Outline each blood parasite and name the species.
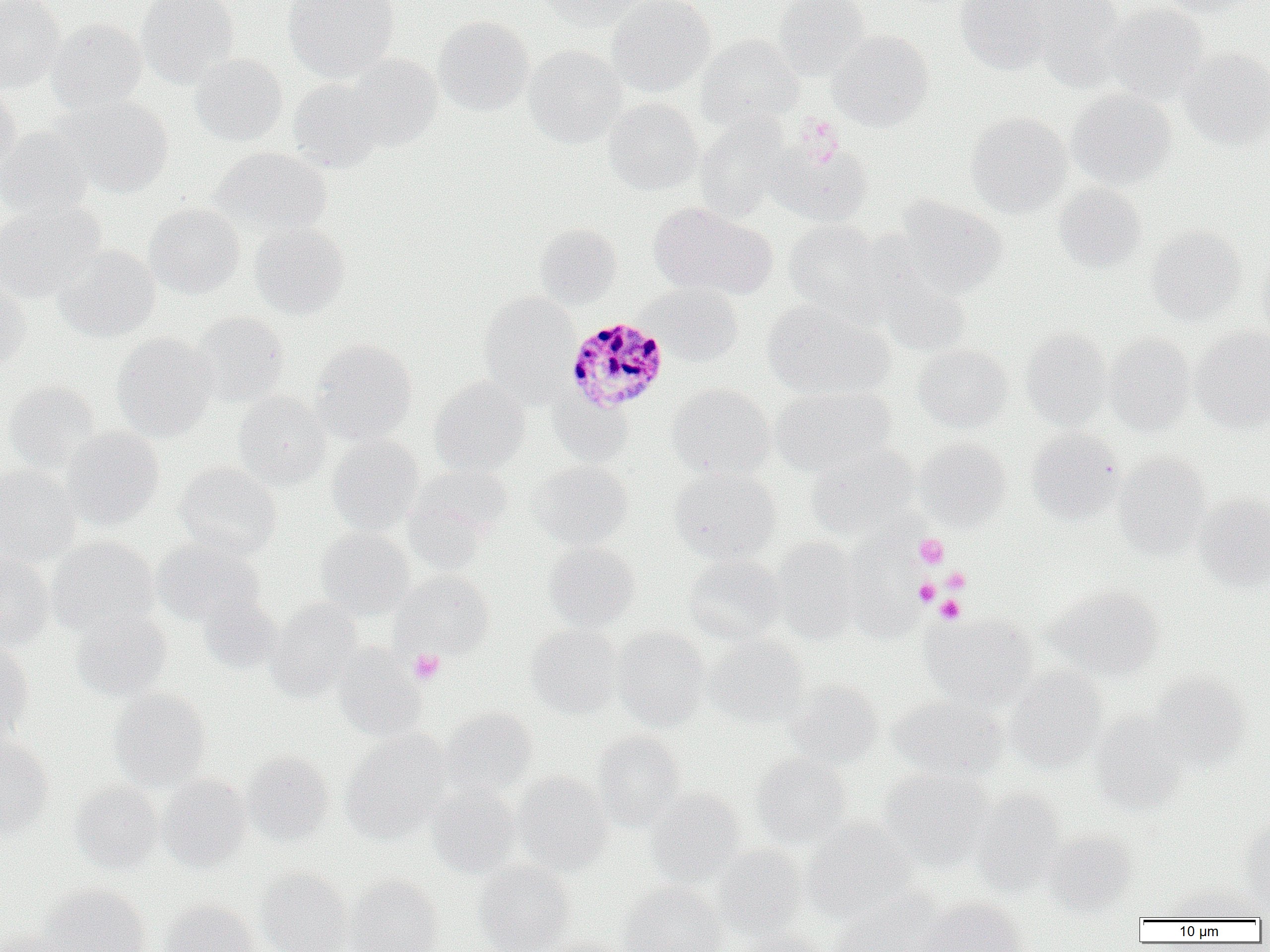

Approximate bounding boxes as [x1, y1, x2, y2] in pixels.
Plasmodium malariae-infected red blood cells: [565, 316, 669, 414].
No Plasmodium falciparum, Plasmodium ovale, Plasmodium vivax, Babesia divergens, or Trypanosoma brucei observed.

Platelet locations: [795, 116, 845, 166], [914, 533, 949, 569], [941, 568, 970, 593], [914, 578, 939, 606], [935, 596, 964, 623], [409, 648, 445, 684]. Uninfected red blood cell locations: [0, 0, 64, 94], [135, 0, 240, 88], [282, 0, 400, 82], [536, 0, 651, 29], [606, 0, 716, 97], [773, 0, 870, 81], [956, 0, 1053, 74], [1029, 0, 1126, 88], [1159, 0, 1263, 17], [1102, 3, 1209, 105], [433, 17, 534, 116], [48, 19, 147, 113], [828, 30, 933, 130], [696, 34, 803, 130], [524, 45, 628, 148], [1179, 48, 1270, 150], [189, 54, 287, 146], [344, 55, 443, 152], [287, 78, 384, 172], [0, 84, 21, 176], [1067, 89, 1176, 190], [53, 96, 173, 197], [603, 98, 703, 195], [966, 111, 1071, 217], [696, 115, 792, 221], [0, 127, 95, 220], [770, 140, 873, 226], [210, 146, 331, 237], [1054, 183, 1147, 272], [894, 197, 1008, 297], [0, 200, 105, 303], [649, 201, 775, 300], [145, 203, 245, 298], [783, 219, 888, 318], [249, 222, 349, 319], [534, 223, 621, 309], [1147, 226, 1247, 325], [53, 245, 159, 342], [1256, 249, 1270, 341], [0, 276, 31, 368], [876, 276, 973, 357], [641, 282, 744, 366], [478, 292, 579, 400], [763, 300, 894, 400], [191, 312, 289, 407], [1191, 326, 1270, 430], [1021, 329, 1112, 430], [112, 332, 218, 441], [1104, 333, 1196, 435], [311, 339, 417, 444], [913, 343, 1013, 431], [430, 376, 530, 476], [3, 380, 100, 474], [666, 383, 775, 480], [771, 386, 896, 476], [233, 390, 331, 490], [551, 393, 633, 466], [60, 427, 164, 529], [1027, 429, 1123, 524], [326, 435, 424, 536], [914, 438, 1011, 530], [807, 444, 919, 540], [1112, 454, 1212, 556], [531, 460, 633, 550], [175, 462, 281, 558], [0, 465, 81, 566], [410, 465, 514, 545], [669, 467, 781, 565], [402, 491, 493, 571], [1195, 494, 1270, 590], [316, 528, 413, 619], [47, 535, 160, 636], [153, 537, 265, 626], [771, 537, 862, 645], [840, 539, 925, 642], [544, 542, 640, 630], [0, 552, 54, 652], [683, 555, 786, 645], [392, 570, 494, 658], [1046, 585, 1164, 681], [198, 595, 282, 674], [266, 598, 363, 701], [70, 609, 172, 701], [924, 613, 1037, 709], [526, 624, 623, 717], [613, 627, 710, 731], [705, 635, 809, 728], [0, 640, 34, 741], [332, 646, 426, 741], [1005, 666, 1107, 770], [1149, 673, 1251, 771], [785, 681, 884, 769], [109, 689, 211, 790], [889, 695, 1008, 782], [439, 708, 538, 799], [1090, 710, 1188, 814], [341, 730, 451, 842], [591, 731, 685, 831], [0, 737, 53, 836], [242, 751, 334, 846], [752, 754, 851, 849], [878, 768, 993, 869], [512, 771, 613, 876], [158, 774, 251, 871], [70, 782, 163, 874], [426, 784, 521, 877], [645, 788, 745, 887], [971, 788, 1065, 895], [802, 819, 917, 923], [1238, 821, 1270, 910], [1043, 831, 1136, 915], [711, 844, 807, 940], [474, 860, 575, 952], [256, 868, 351, 952], [346, 875, 444, 952], [618, 882, 726, 952], [41, 883, 150, 952], [1167, 883, 1263, 921], [828, 890, 945, 951], [913, 897, 1028, 952], [160, 900, 260, 952], [0, 926, 67, 952], [726, 930, 828, 952], [540, 935, 631, 952]. Slide-level diagnosis: Plasmodium malariae. Thin blood film. One field of a larger specimen. Light microscopy. Captured at 1000x magnification. Image is 1270×952 pixels.